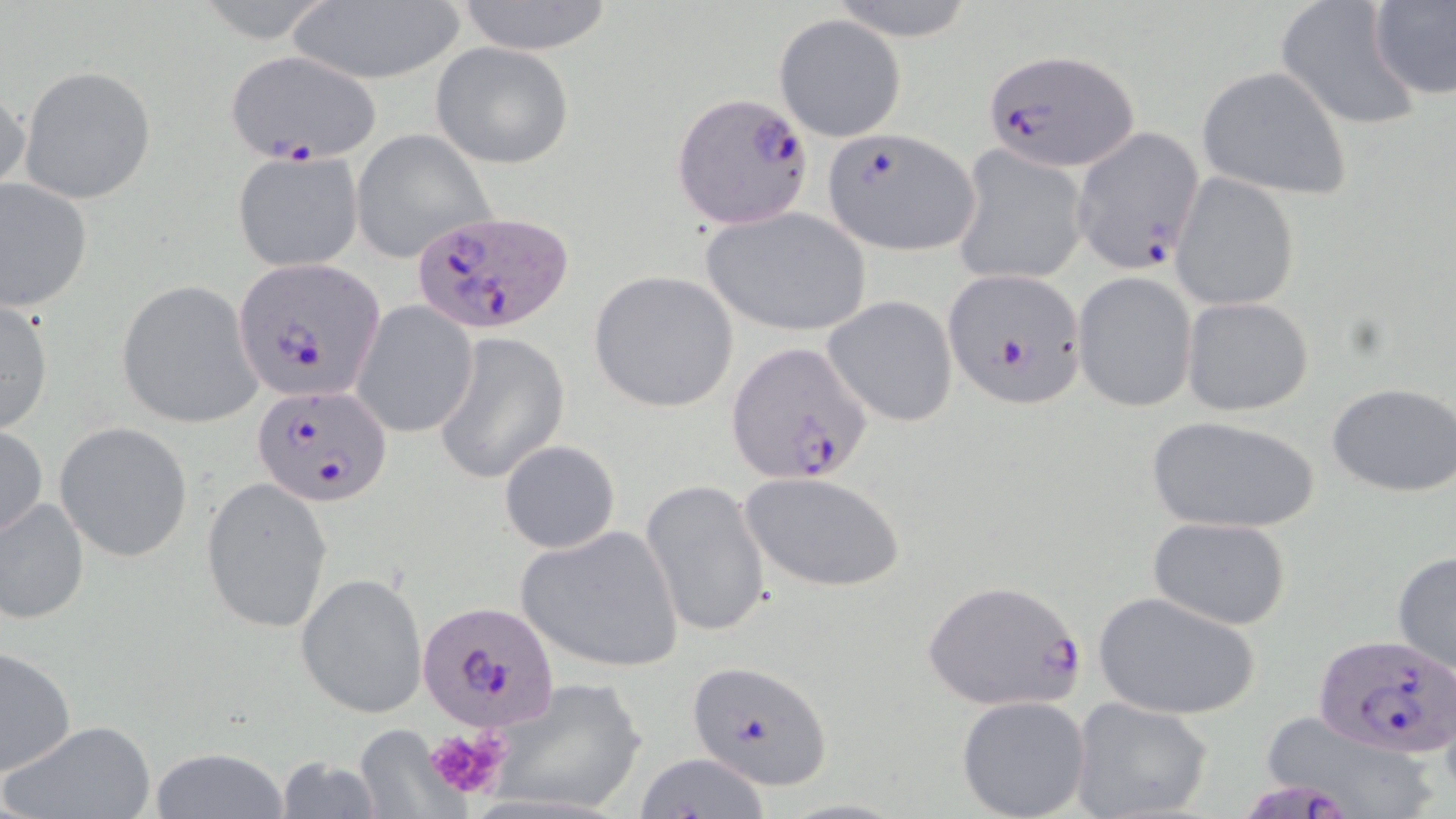 Approximate bounding boxes as (x1,y1)-(x2,y2) corner pairs in pixels. Plasmodium falciparum-infected red blood cell locations: (982,47)-(1140,173), (225,48)-(378,165), (670,91)-(814,232), (819,128)-(980,257), (1070,128)-(1206,275), (409,210)-(578,336), (234,258)-(385,403), (943,269)-(1088,410), (727,339)-(875,485), (250,383)-(394,507), (920,579)-(1088,712), (418,602)-(558,734), (1316,631)-(1456,756), (686,661)-(834,791). Platelet locations: (422,726)-(510,800). Uninfected red blood cell locations: (451,0)-(618,55), (825,0)-(979,40), (1370,0)-(1456,101), (286,2)-(466,85), (1275,2)-(1421,130), (775,13)-(905,141), (429,42)-(574,169), (19,66)-(156,203), (1196,66)-(1354,200), (0,80)-(31,200), (352,131)-(495,263), (951,146)-(1090,287), (231,150)-(363,272), (1170,173)-(1300,311), (0,176)-(94,313), (700,207)-(872,339), (589,270)-(739,413), (1072,272)-(1198,414), (116,280)-(263,427), (823,295)-(960,428), (1181,296)-(1315,417), (0,298)-(54,434), (354,301)-(478,438), (434,331)-(570,486), (1326,382)-(1456,497), (1146,414)-(1320,534), (54,422)-(192,562), (1,424)-(48,542), (499,439)-(621,554), (738,470)-(906,592), (200,476)-(333,634), (641,478)-(771,638), (1,496)-(89,626), (1149,516)-(1293,631), (515,526)-(684,674), (1391,549)-(1456,679), (296,570)-(429,719), (1094,591)-(1261,720), (1,646)-(76,775), (487,675)-(648,815), (956,695)-(1090,819), (1068,698)-(1213,819), (1252,710)-(1447,819), (5,719)-(157,819), (352,730)-(469,818), (145,747)-(291,819), (631,754)-(776,818), (272,757)-(387,817). Slide-level diagnosis: Plasmodium falciparum. Thin blood smear. Image is 1456×819 pixels. One field of a larger specimen. May-Grünwald-Giemsa-stained preparation. 1000x magnification. Light microscopy.